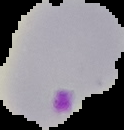

Cell region segmented out of the field of view; the surrounding area is masked to black. Image is 124×130 pixels. From a thin blood film. Result: Plasmodium parasites detected.